Identify the parasite.
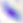

This is Toxoplasma gondii.

Summary:
  - Modality: photomicrograph
  - Magnification: 400x